Locate and identify every blood parasite.
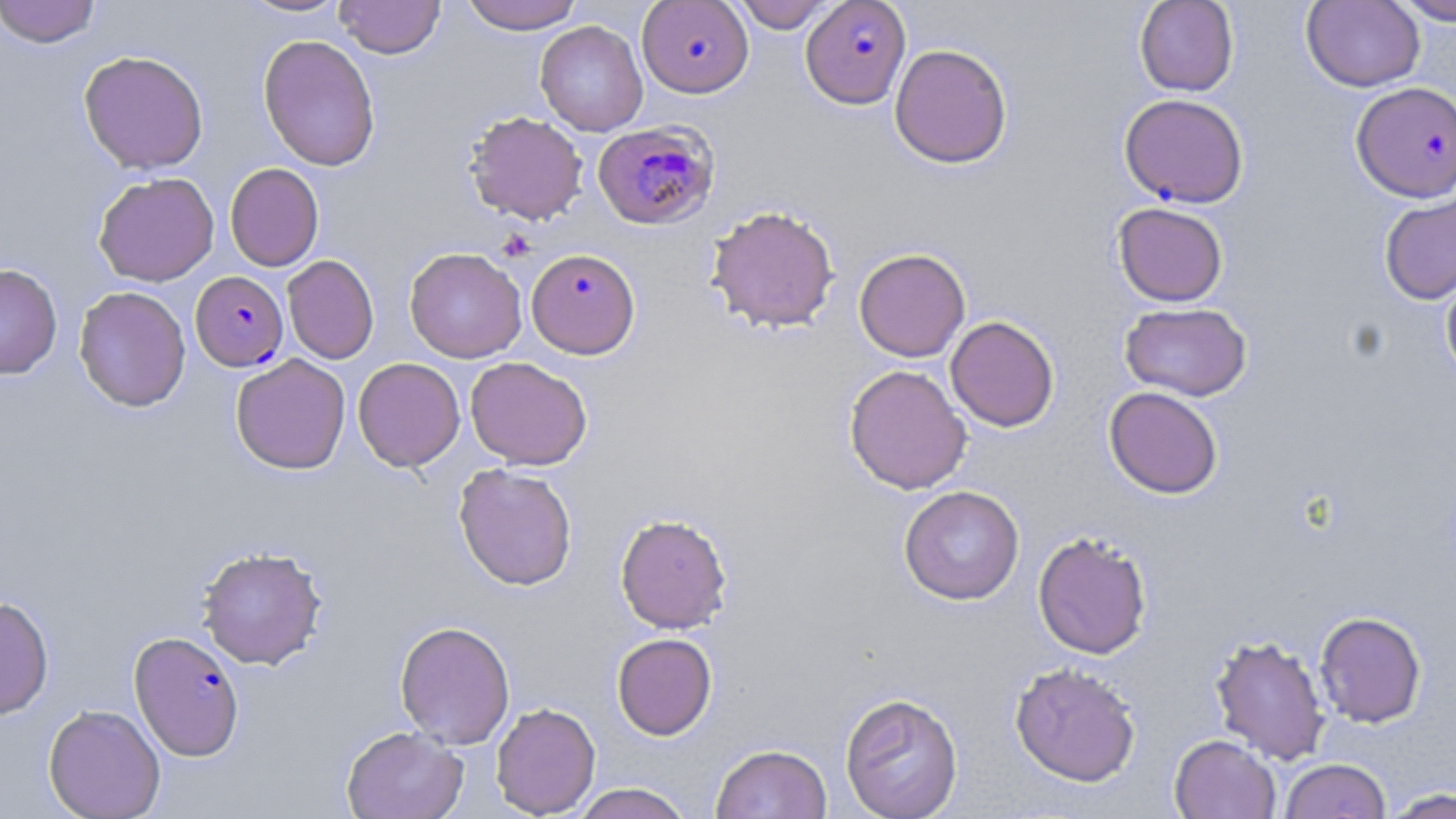

Approximate bounding boxes as (x1, y1, x2, y2) in pixels.
Plasmodium falciparum-infected red blood cells: (637, 0, 754, 98), (802, 0, 914, 111), (1351, 81, 1456, 203), (1119, 93, 1248, 208), (592, 120, 720, 230), (526, 248, 641, 359), (191, 271, 288, 371), (129, 631, 245, 761).
No Plasmodium ovale, Plasmodium malariae, Plasmodium vivax, Babesia divergens, or Trypanosoma brucei observed.

Uninfected red blood cell locations: (0, 0, 102, 47), (237, 0, 352, 18), (336, 0, 445, 59), (459, 0, 585, 34), (732, 0, 837, 33), (1135, 0, 1239, 96), (1390, 0, 1456, 25), (1301, 1, 1425, 93), (535, 20, 648, 136), (258, 34, 381, 171), (889, 43, 1013, 169), (78, 50, 209, 174), (464, 111, 588, 225), (225, 163, 324, 271), (93, 171, 219, 287), (1379, 188, 1456, 306), (1112, 202, 1228, 307), (705, 204, 840, 333), (404, 246, 527, 363), (854, 247, 971, 362), (282, 255, 379, 364), (0, 263, 62, 379), (1440, 266, 1456, 386), (74, 285, 191, 412), (1119, 301, 1251, 401), (945, 315, 1060, 432), (230, 354, 351, 474), (466, 356, 592, 470), (353, 357, 465, 471), (844, 364, 972, 495), (1104, 386, 1223, 499), (453, 463, 578, 591), (898, 485, 1024, 605), (615, 513, 732, 633), (1033, 530, 1152, 660), (196, 545, 328, 670), (0, 595, 55, 720), (1314, 610, 1427, 728), (394, 620, 515, 748), (612, 633, 717, 740), (1209, 634, 1331, 765), (1009, 661, 1142, 787), (839, 692, 964, 818), (490, 702, 601, 817), (43, 703, 166, 819), (341, 726, 468, 819), (1169, 734, 1280, 819), (711, 743, 832, 819), (1279, 758, 1391, 818), (570, 783, 694, 819), (1383, 787, 1456, 818). Slide-level diagnosis: Plasmodium falciparum. Thin blood film. Single field of view. Image is 1456×819 pixels. Light microscopy. May-Grünwald-Giemsa stain. Captured at 1000x magnification.